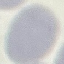

Result: negative for malaria parasites. Photographed with a smartphone camera at the microscope eyepiece. Thin blood film. Giemsa stain. Cell patch, automatically extracted from a larger field of view and resized to 64 × 64 pixels.